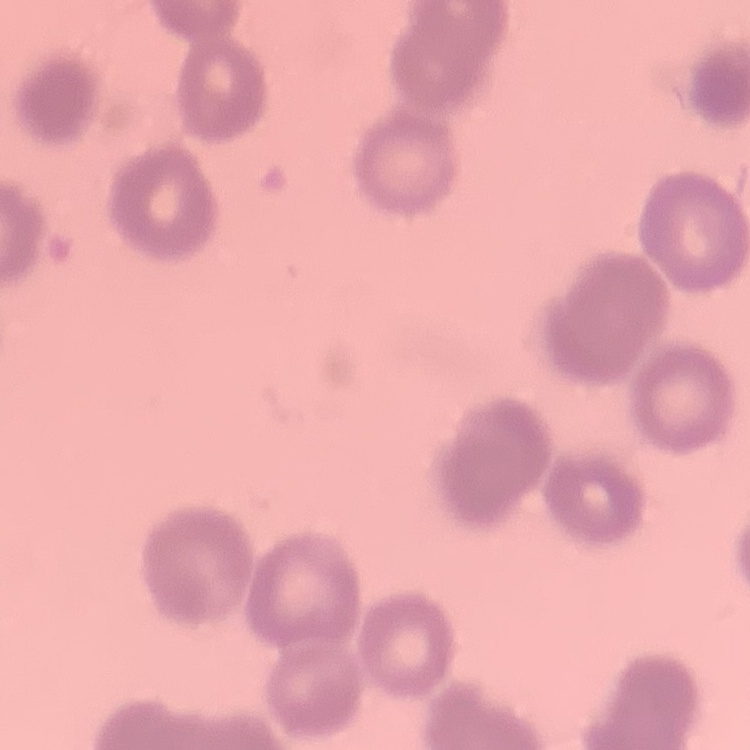

The red blood cells show rouleaux formation. Thin blood film. One tile cut from a larger photomicrograph. Field's or Giemsa stain.